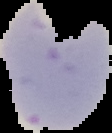
Result: Plasmodium parasites identified. From a thin blood film. Cell region segmented out of the field of view; the surrounding area is masked to black. Image is 112×133 pixels.